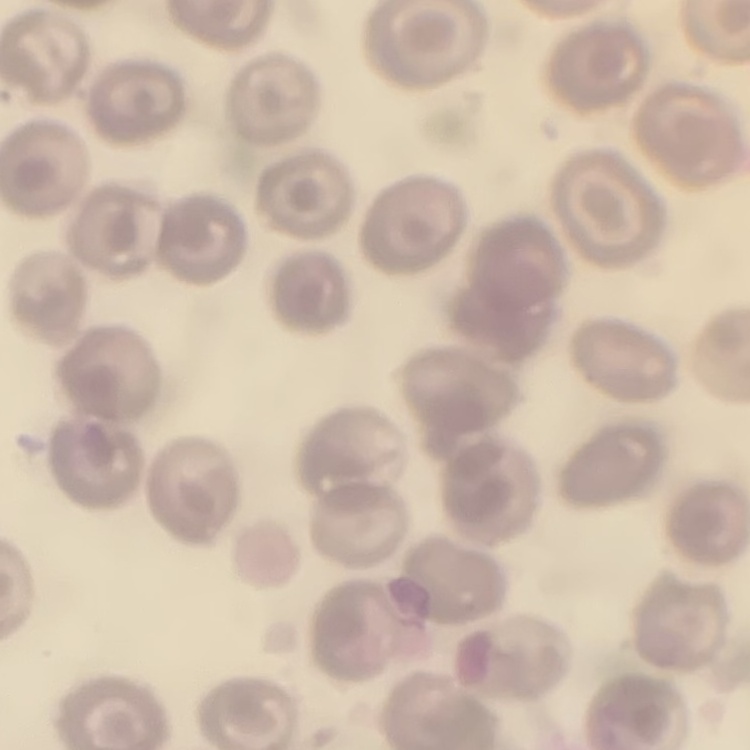
red blood cell morphology = no rouleaux formation
image type = one tile cut from a larger photomicrograph
preparation = thin peripheral smear
stain = Field's or Giemsa